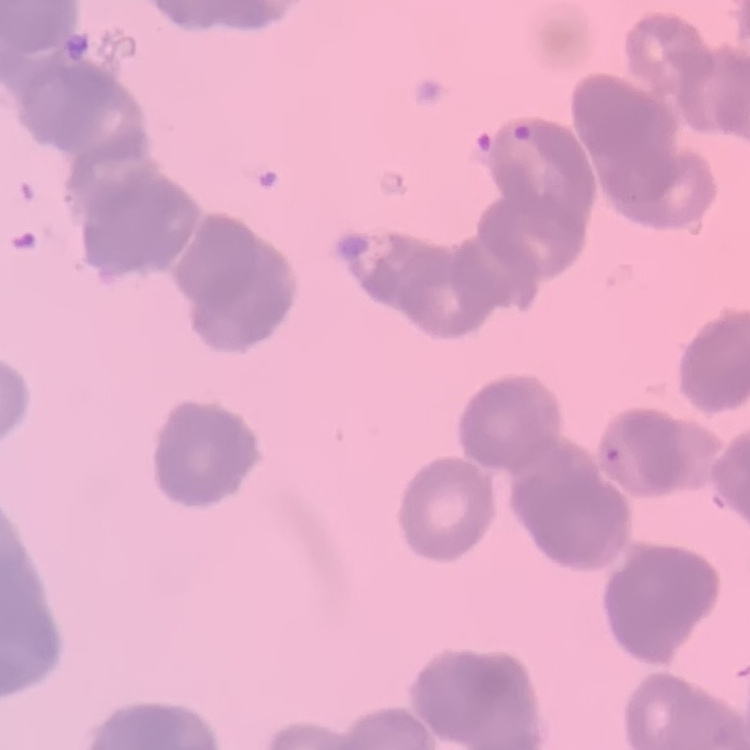 The red blood cells exhibit rouleaux formation. Field's or Giemsa stain. Thin peripheral smear. Square crop of a larger photomicrograph.